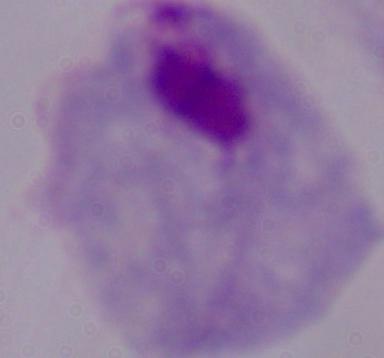

modality = micrograph
magnification = 1000x
identification = trichomonad